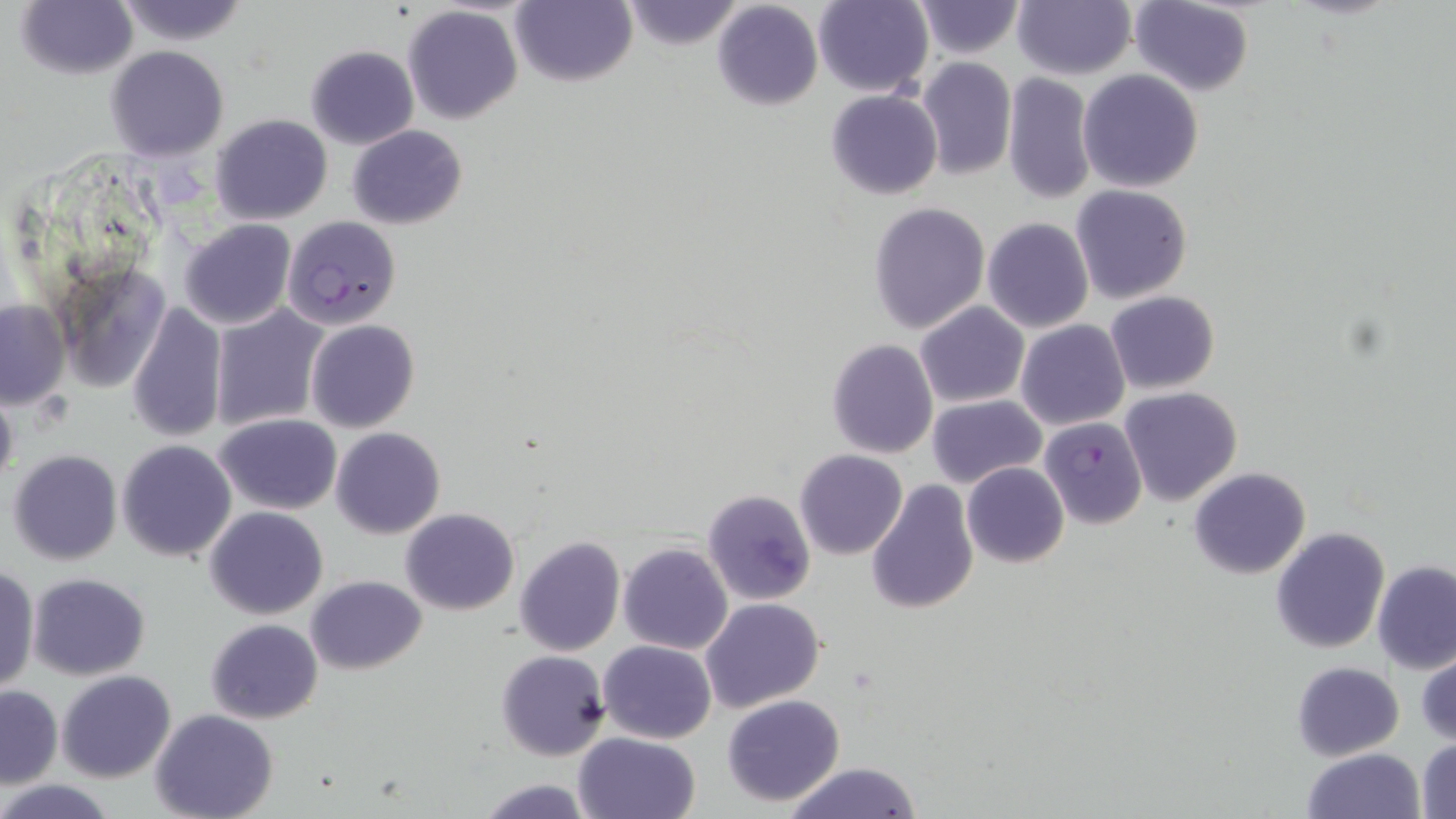

slide_level_diagnosis: Plasmodium falciparum
uninfected_red_blood_cell_locations: 'approximate bounding boxes as (x1,y1)-(x2,y2) corner pairs in pixels: (15,0)-(139,81), (113,0)-(251,46), (510,0)-(636,87), (1013,0)-(1136,79), (1129,0)-(1255,96), (620,1)-(747,52), (713,1)-(822,111), (812,1)-(934,97), (911,1)-(1026,57), (402,6)-(524,126), (305,44)-(418,149), (105,46)-(229,161), (916,57)-(1016,179), (1079,69)-(1203,192), (1002,73)-(1097,206), (826,89)-(943,199), (210,113)-(332,225), (348,125)-(467,230), (1070,184)-(1194,305), (868,201)-(990,333), (982,218)-(1094,334), (178,219)-(297,330), (54,261)-(175,393), (1105,290)-(1219,394), (0,300)-(69,409), (126,300)-(228,443), (916,302)-(1029,408), (210,306)-(328,430), (305,319)-(419,433), (1016,319)-(1130,430), (826,338)-(938,458), (0,381)-(17,497), (1120,386)-(1242,505), (927,395)-(1047,488), (215,414)-(341,515), (331,427)-(445,539), (117,439)-(238,560), (7,449)-(123,566), (794,449)-(907,560), (962,462)-(1069,568), (1189,467)-(1311,579), (866,478)-(979,615), (702,489)-(816,605), (1229,492)-(1375,626), (205,507)-(328,619), (400,507)-(520,615), (1270,527)-(1390,653), (514,535)-(625,657), (618,543)-(733,654), (1373,561)-(1455,673), (0,565)-(38,695), (27,573)-(150,680), (306,575)-(427,674), (700,598)-(824,714), (206,619)-(323,724), (598,640)-(716,744), (1417,650)-(1455,745), (497,651)-(610,760), (1290,661)-(1404,762), (57,669)-(177,782), (1,686)-(61,789), (722,694)-(846,807), (150,710)-(278,819), (574,731)-(700,818), (1415,738)-(1456,818), (1301,748)-(1424,819), (782,762)-(923,819), (477,778)-(595,818), (2,779)-(117,817)'
magnification: 1000x
preparation: thin blood smear
stain: May-Grünwald-Giemsa
field_of_view: one of a larger specimen
plasmodium_falciparum_infected_red_blood_cell_locations: 'approximate bounding boxes as (x1,y1)-(x2,y2) corner pairs in pixels: (282,217)-(401,331), (1039,416)-(1148,529)'
modality: optical microscopy
image_size: 1456×819 pixels